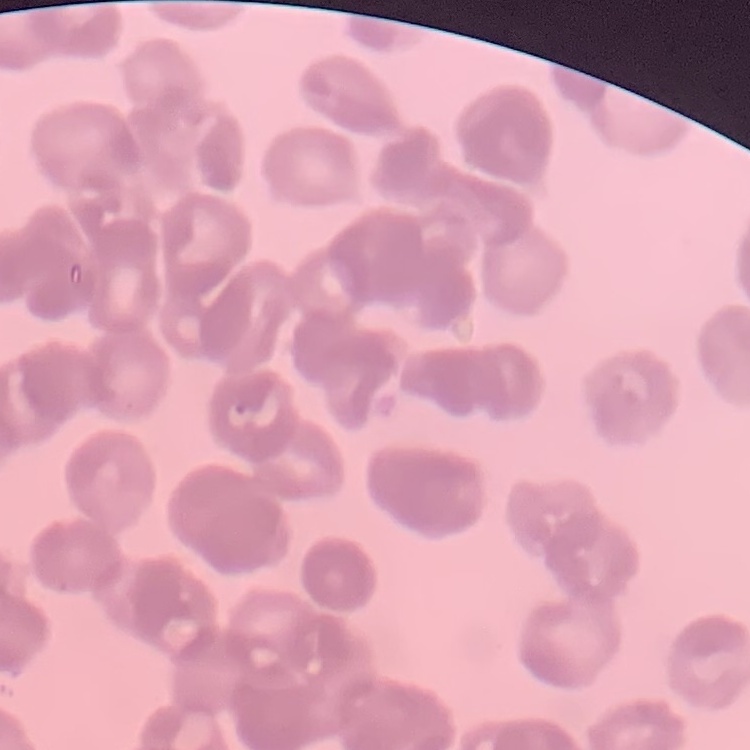
erythrocyte morphology = rouleaux formation
image type = one tile cut from a larger photomicrograph
stain = Field's or Giemsa
preparation = thin blood smear